Report the malaria status of this cell.
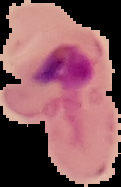

Parasitized.

image size = 121×187 pixels
image type = segmented cell region with the area outside set to black
preparation = thin blood smear